Locate every Plasmodium malariae-infected red blood cell.
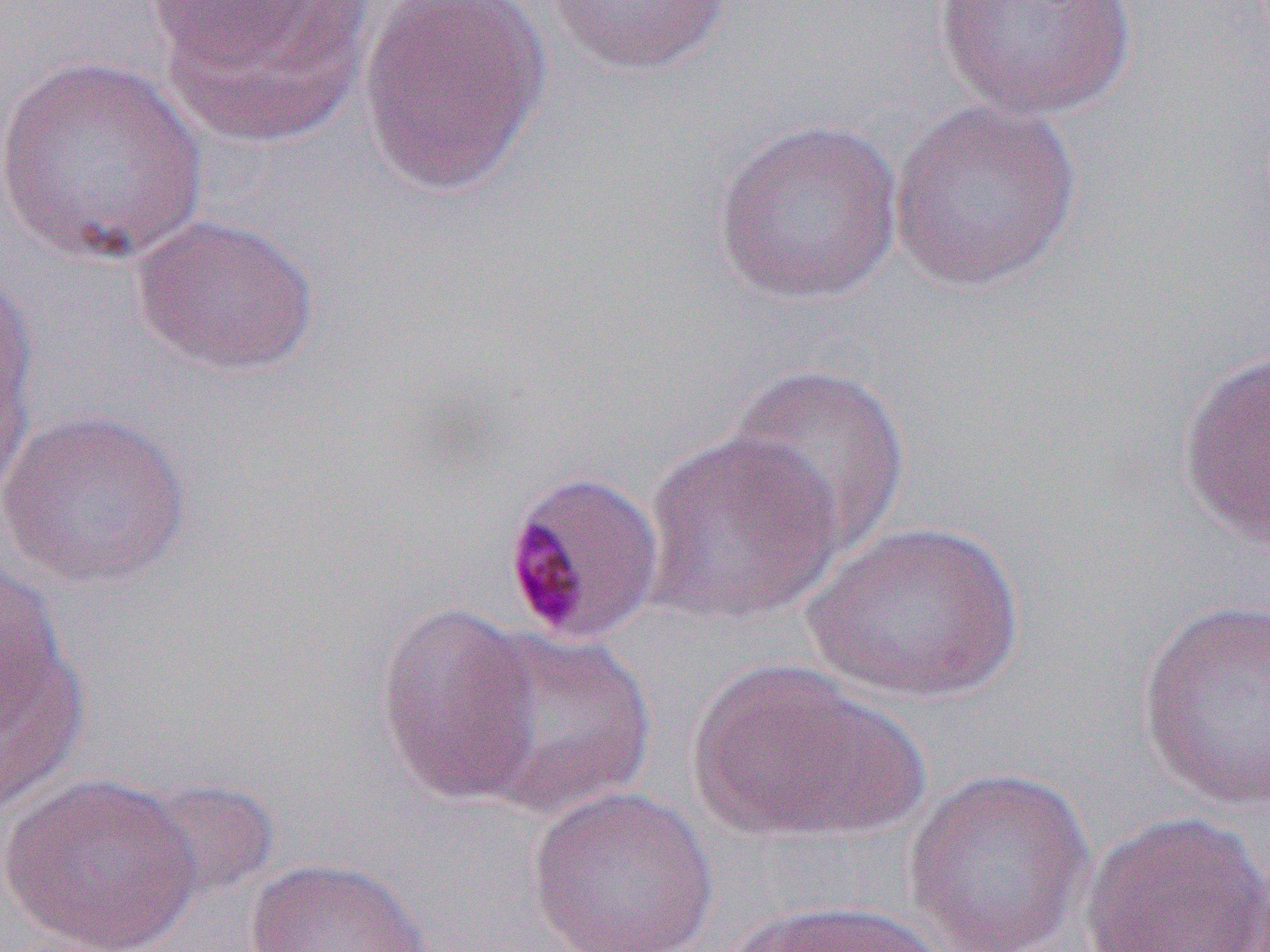

Approximate bounding boxes as (x1, y1, x2, y2) in pixels.
Plasmodium malariae-infected red blood cells: (501, 468, 666, 647).

Uninfected red blood cell locations: (358, 0, 553, 194), (545, 0, 734, 76), (931, 0, 1139, 121), (148, 2, 379, 145), (0, 54, 212, 267), (887, 99, 1084, 293), (712, 118, 903, 305), (133, 213, 319, 377), (0, 277, 38, 510), (1176, 346, 1269, 549), (722, 361, 912, 559), (0, 408, 192, 590), (640, 432, 844, 627), (803, 520, 1023, 707), (0, 557, 68, 728), (1137, 599, 1269, 811), (372, 601, 544, 806), (461, 628, 657, 820), (0, 638, 90, 814), (686, 658, 915, 843), (902, 767, 1095, 950), (2, 772, 202, 952), (138, 777, 281, 903), (526, 785, 719, 952), (1079, 810, 1269, 952), (243, 856, 434, 952), (723, 898, 951, 952). Slide-level diagnosis: Plasmodium malariae. Thin blood smear. Optical microscopy. One field of a larger specimen. Image is 1270×952 pixels. Captured at 1000x magnification.